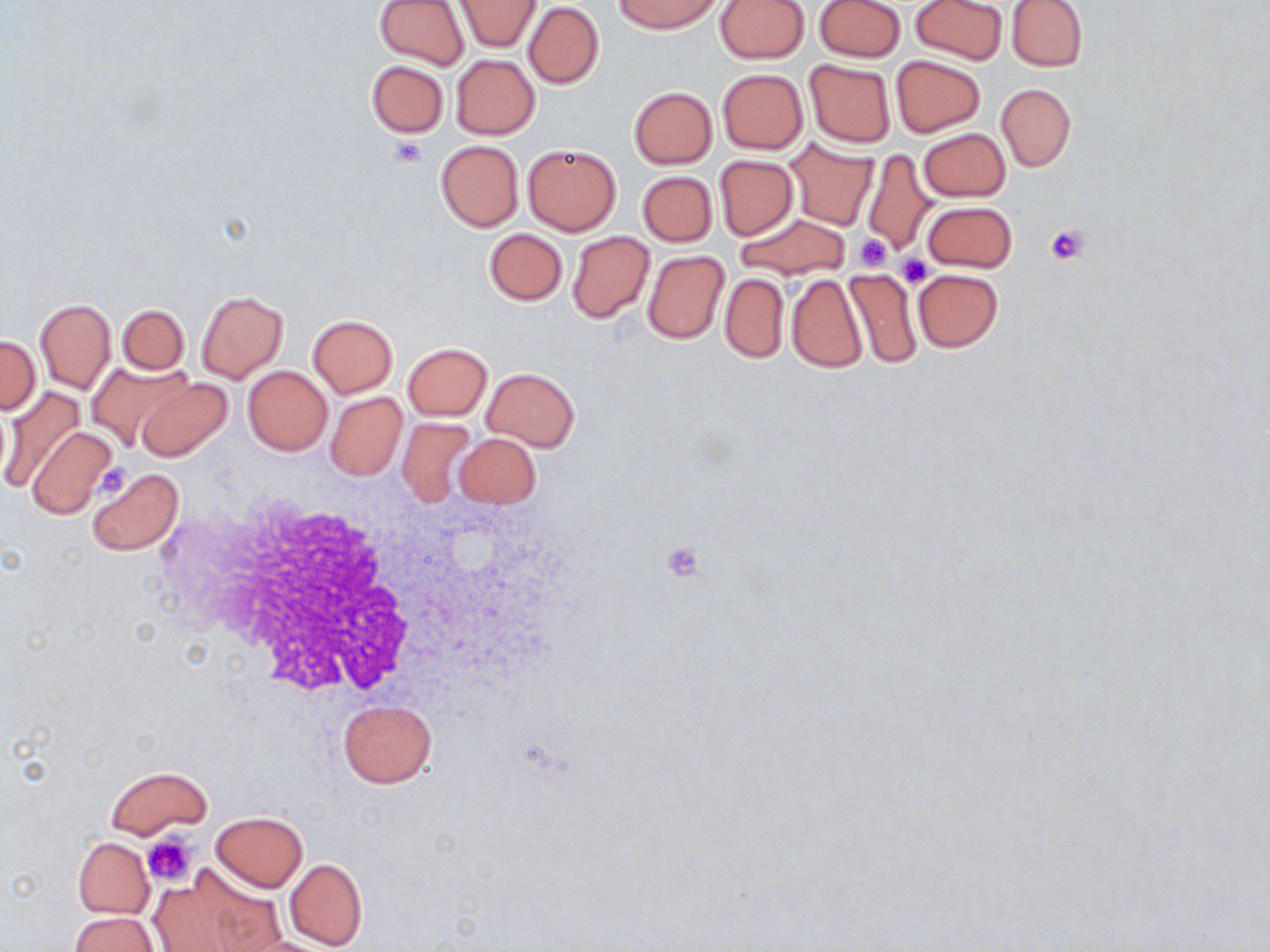

Approximate bounding boxes as (x1,y1)-(x2,y2) corner pairs in pixels. Uninfected red blood cell locations: (375,0)-(470,70), (455,0)-(540,51), (615,0)-(721,34), (714,0)-(810,62), (815,0)-(904,63), (911,0)-(1007,64), (1006,0)-(1088,72), (523,3)-(603,88), (450,55)-(539,138), (890,55)-(985,135), (804,59)-(896,148), (365,60)-(449,138), (717,69)-(808,153), (997,84)-(1075,171), (629,87)-(717,168), (917,128)-(1010,201), (435,140)-(523,231), (785,140)-(878,229), (522,144)-(621,235), (861,150)-(938,259), (714,155)-(799,240), (637,170)-(717,247), (923,201)-(1017,273), (734,213)-(850,279), (484,228)-(567,305), (566,231)-(655,323), (641,250)-(729,345), (911,268)-(1002,352), (843,269)-(922,368), (719,273)-(788,362), (785,273)-(868,373), (195,291)-(287,383), (35,299)-(114,393), (117,304)-(189,373), (307,314)-(397,397), (0,336)-(41,414), (403,342)-(492,420), (87,359)-(192,451), (243,367)-(332,454), (482,367)-(580,451), (134,376)-(233,462), (0,384)-(84,495), (326,391)-(407,481), (396,417)-(477,507), (25,426)-(118,520), (453,433)-(541,508), (86,467)-(184,557), (337,700)-(437,787), (105,766)-(212,841), (211,812)-(308,892), (73,837)-(153,918), (283,857)-(367,951), (150,863)-(275,952), (69,912)-(158,952). Platelet locations: (390,137)-(428,169), (1045,223)-(1090,264), (855,233)-(893,271), (900,253)-(932,287), (95,461)-(132,502), (661,540)-(708,582), (143,834)-(197,886). White blood cell locations: (145,489)-(422,700). Slide-level diagnosis: negative for blood parasites. Captured at 1000x magnification. Image is 1270×952 pixels. May-Grünwald-Giemsa-stained preparation. Light microscopy. Thin blood smear. Single field of view.